Comment on the morphology of the erythrocytes.
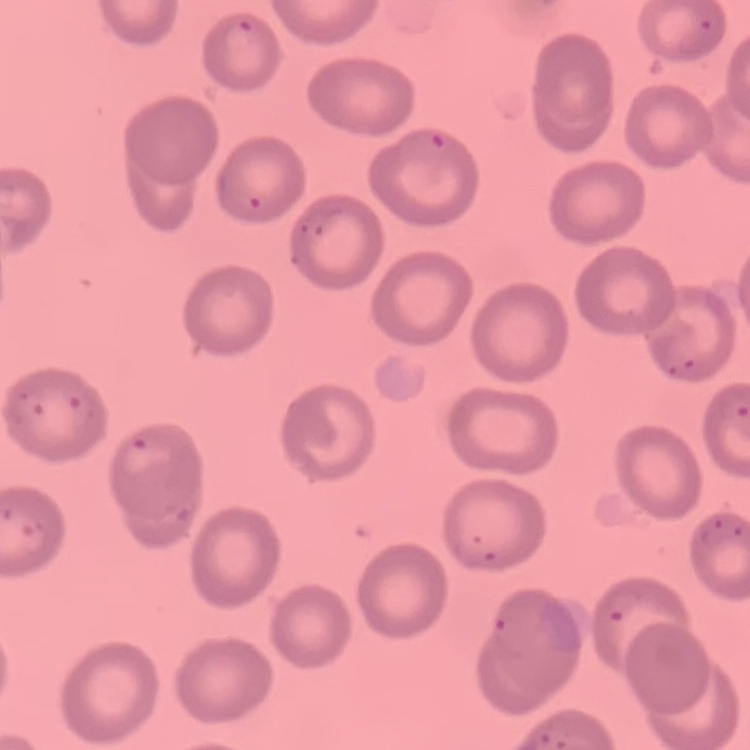

They show no rouleaux formation.

Summary:
  - Stain: Field's or Giemsa
  - Preparation: thin blood film
  - Image type: square crop of a larger photomicrograph